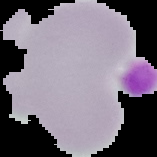

result = no Plasmodium parasites seen
image size = 157×157 pixels
preparation = thin blood smear
image type = segmented cell region with the area outside set to black